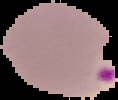 From a thin blood film. Malaria status: parasitized. Segmented cell region on a black background. Image is 118×100 pixels.